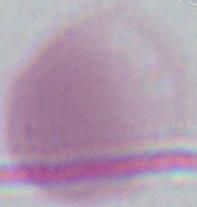

Summary:
  - Modality: photomicrograph
  - Identification: erythrocyte
  - Magnification: 1000x